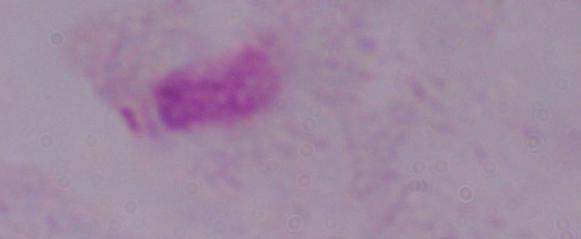

A trichomonad is seen. Photomicrograph. Captured at 1000x magnification.